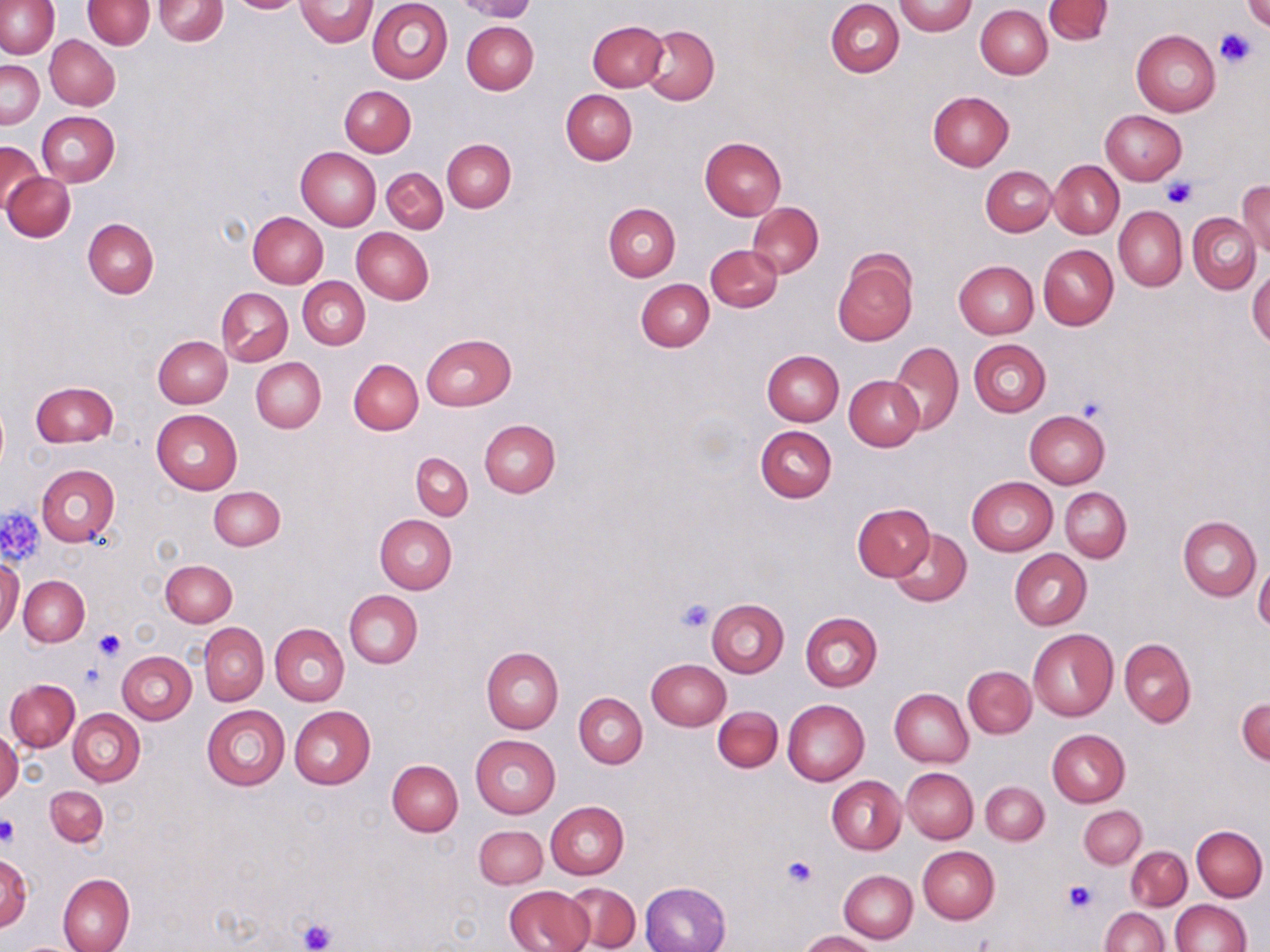

{
  "slide_level_diagnosis": "negative for blood parasites",
  "field_of_view": "one of a larger specimen",
  "stain": "May-Grünwald-Giemsa",
  "modality": "light microscopy",
  "magnification": "1000x",
  "uninfected_red_blood_cell_locations": "approximate bounding boxes as named x1/y1/x2/y2 corners in pixels: (x1=82, y1=0, x2=154, y2=48), (x1=154, y1=0, x2=227, y2=46), (x1=225, y1=0, x2=307, y2=14), (x1=295, y1=0, x2=378, y2=46), (x1=366, y1=0, x2=453, y2=84), (x1=456, y1=0, x2=536, y2=22), (x1=827, y1=0, x2=904, y2=77), (x1=1044, y1=0, x2=1113, y2=44), (x1=0, y1=1, x2=59, y2=58), (x1=895, y1=1, x2=976, y2=36), (x1=1241, y1=1, x2=1270, y2=33), (x1=976, y1=5, x2=1052, y2=79), (x1=587, y1=20, x2=668, y2=91), (x1=462, y1=21, x2=539, y2=95), (x1=640, y1=24, x2=719, y2=103), (x1=1132, y1=30, x2=1220, y2=116), (x1=45, y1=35, x2=120, y2=109), (x1=1, y1=58, x2=44, y2=128), (x1=339, y1=86, x2=416, y2=156), (x1=560, y1=88, x2=637, y2=165), (x1=928, y1=91, x2=1013, y2=171), (x1=1101, y1=110, x2=1187, y2=184), (x1=36, y1=111, x2=119, y2=187), (x1=700, y1=137, x2=786, y2=220), (x1=443, y1=139, x2=516, y2=212), (x1=0, y1=141, x2=43, y2=214), (x1=295, y1=146, x2=381, y2=229), (x1=1049, y1=159, x2=1124, y2=239), (x1=981, y1=166, x2=1057, y2=237), (x1=381, y1=167, x2=448, y2=234), (x1=3, y1=172, x2=75, y2=242), (x1=1238, y1=182, x2=1270, y2=257), (x1=603, y1=202, x2=680, y2=281), (x1=748, y1=202, x2=823, y2=278), (x1=1114, y1=206, x2=1186, y2=291), (x1=249, y1=211, x2=329, y2=287), (x1=1189, y1=214, x2=1261, y2=293), (x1=83, y1=218, x2=159, y2=299), (x1=351, y1=229, x2=433, y2=305), (x1=705, y1=244, x2=783, y2=312), (x1=1038, y1=245, x2=1118, y2=329), (x1=832, y1=250, x2=917, y2=346), (x1=954, y1=260, x2=1038, y2=338), (x1=1248, y1=267, x2=1270, y2=350), (x1=299, y1=277, x2=369, y2=349), (x1=636, y1=278, x2=714, y2=351), (x1=217, y1=287, x2=293, y2=366), (x1=421, y1=334, x2=517, y2=410), (x1=153, y1=336, x2=232, y2=408), (x1=969, y1=338, x2=1051, y2=416), (x1=887, y1=341, x2=963, y2=435), (x1=762, y1=350, x2=844, y2=425), (x1=251, y1=357, x2=326, y2=432), (x1=349, y1=359, x2=423, y2=434), (x1=844, y1=375, x2=924, y2=452), (x1=30, y1=381, x2=118, y2=447), (x1=151, y1=408, x2=243, y2=494), (x1=1024, y1=410, x2=1110, y2=489), (x1=480, y1=419, x2=560, y2=497), (x1=756, y1=425, x2=836, y2=502), (x1=412, y1=452, x2=473, y2=519), (x1=36, y1=464, x2=119, y2=546), (x1=967, y1=476, x2=1057, y2=556), (x1=210, y1=487, x2=284, y2=550), (x1=1060, y1=487, x2=1131, y2=563), (x1=853, y1=503, x2=932, y2=581), (x1=374, y1=514, x2=457, y2=593), (x1=1178, y1=517, x2=1260, y2=601), (x1=888, y1=528, x2=972, y2=607), (x1=1009, y1=549, x2=1091, y2=629), (x1=1, y1=558, x2=23, y2=638), (x1=160, y1=559, x2=237, y2=627), (x1=1255, y1=562, x2=1270, y2=634), (x1=19, y1=575, x2=89, y2=646), (x1=345, y1=590, x2=423, y2=668), (x1=706, y1=598, x2=789, y2=676), (x1=800, y1=612, x2=882, y2=692), (x1=198, y1=623, x2=268, y2=705), (x1=271, y1=623, x2=349, y2=706), (x1=1028, y1=628, x2=1118, y2=722), (x1=1119, y1=638, x2=1195, y2=727), (x1=481, y1=647, x2=563, y2=732), (x1=117, y1=652, x2=196, y2=724), (x1=646, y1=659, x2=730, y2=730), (x1=963, y1=666, x2=1035, y2=738), (x1=5, y1=679, x2=80, y2=752), (x1=890, y1=688, x2=972, y2=766), (x1=575, y1=692, x2=647, y2=768), (x1=1237, y1=698, x2=1270, y2=764), (x1=783, y1=699, x2=869, y2=785), (x1=202, y1=705, x2=290, y2=790), (x1=289, y1=706, x2=376, y2=788), (x1=713, y1=706, x2=782, y2=771), (x1=68, y1=710, x2=145, y2=787), (x1=1047, y1=728, x2=1130, y2=807), (x1=1, y1=733, x2=22, y2=805), (x1=470, y1=734, x2=560, y2=819), (x1=387, y1=759, x2=463, y2=836), (x1=901, y1=768, x2=979, y2=843), (x1=827, y1=775, x2=905, y2=854), (x1=981, y1=781, x2=1049, y2=845), (x1=46, y1=785, x2=108, y2=846), (x1=546, y1=800, x2=629, y2=879), (x1=1079, y1=805, x2=1146, y2=868), (x1=474, y1=825, x2=547, y2=887), (x1=1192, y1=825, x2=1267, y2=901), (x1=917, y1=845, x2=999, y2=924), (x1=1125, y1=846, x2=1191, y2=909), (x1=0, y1=856, x2=32, y2=932), (x1=839, y1=869, x2=917, y2=943), (x1=58, y1=873, x2=134, y2=952), (x1=641, y1=881, x2=732, y2=952), (x1=504, y1=884, x2=592, y2=952), (x1=564, y1=884, x2=640, y2=950), (x1=1170, y1=899, x2=1251, y2=951), (x1=1100, y1=907, x2=1169, y2=952), (x1=800, y1=931, x2=877, y2=951)",
  "image_size": "1270×952 pixels",
  "preparation": "thin blood film",
  "platelet_locations": "approximate bounding boxes as named x1/y1/x2/y2 corners in pixels: (x1=1215, y1=28, x2=1258, y2=68), (x1=1161, y1=177, x2=1195, y2=209), (x1=1075, y1=394, x2=1108, y2=426), (x1=1, y1=508, x2=44, y2=561), (x1=676, y1=598, x2=714, y2=633), (x1=91, y1=629, x2=127, y2=661), (x1=0, y1=816, x2=20, y2=845), (x1=782, y1=855, x2=816, y2=889), (x1=1062, y1=881, x2=1094, y2=912), (x1=296, y1=917, x2=338, y2=952)"
}